Locate every malaria parasite.
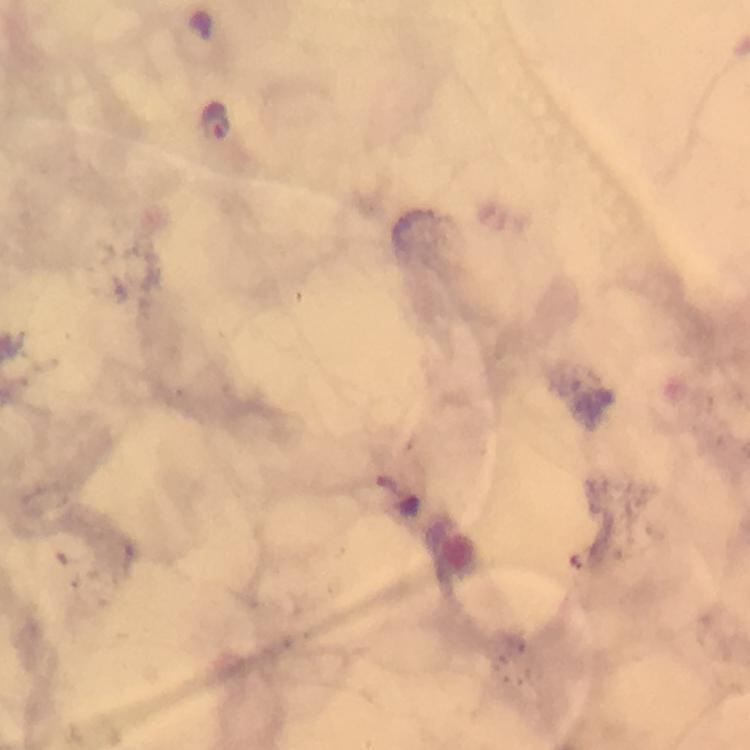

Approximate centers as [x, y] in pixels.
Malaria parasites: [216, 119].

Summary:
  - Preparation: thick blood smear
  - Stain: Giemsa
  - Image size: 750×750 pixels
  - Capture: smartphone photograph through a microscope
  - Magnification: 100x
  - Immersion oil: used
  - Context: from a malaria diagnostic workup
  - Cropped from: a single field of view